Report the malaria status of this cell.
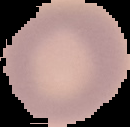

Uninfected.

Image is 130×127 pixels. The area outside the segmented cell region is set to black. From a thin blood smear.